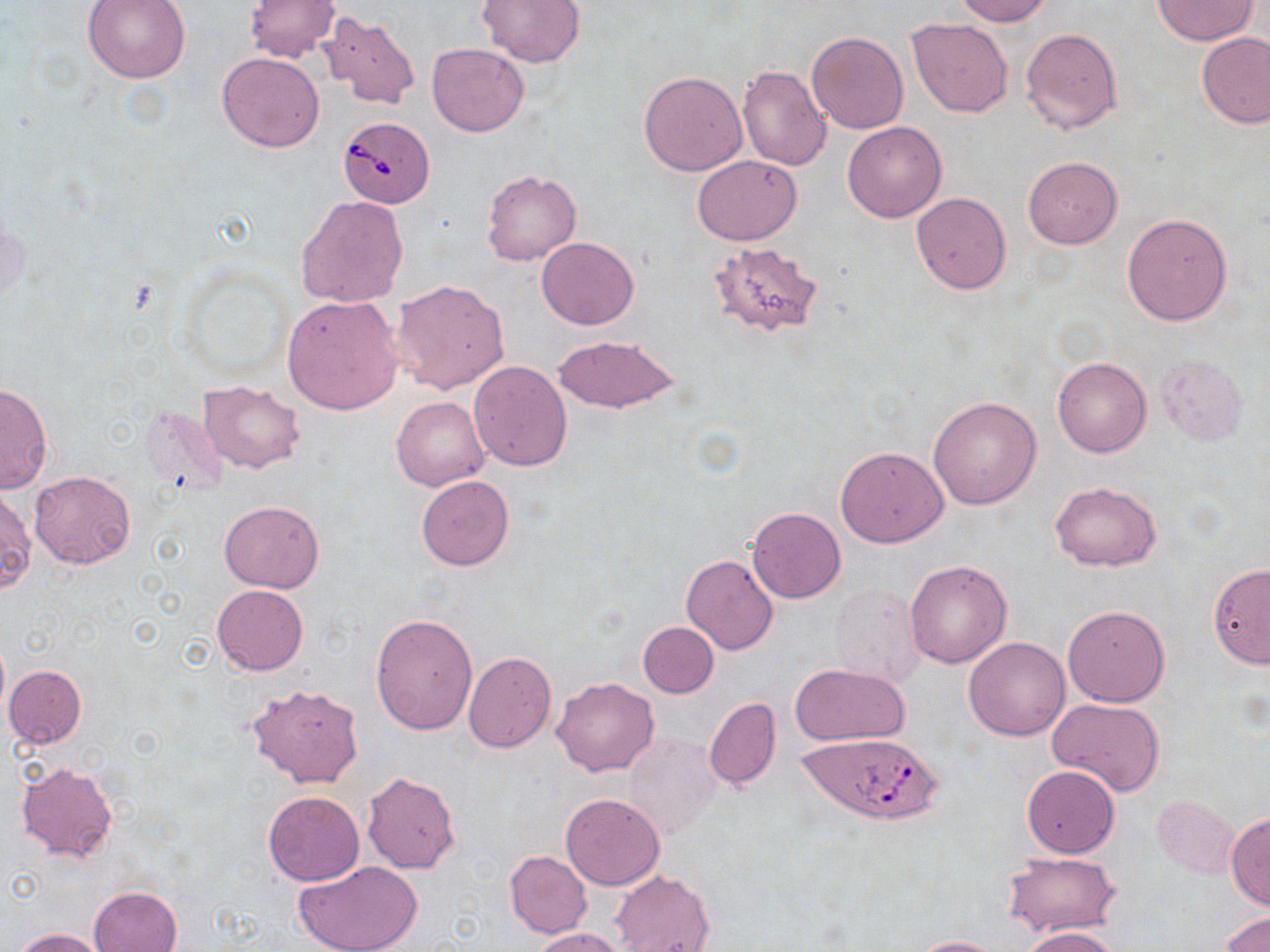

Summary:
  - Coordinate format: approximate bounding boxes as named x1/y1/x2/y2 corners in pixels
  - Babesia divergens-infected red blood cell locations: (x1=339, y1=116, x2=436, y2=208), (x1=800, y1=734, x2=941, y2=825)
  - Uninfected red blood cell locations: (x1=83, y1=0, x2=190, y2=83), (x1=244, y1=0, x2=339, y2=63), (x1=479, y1=0, x2=584, y2=68), (x1=954, y1=0, x2=1051, y2=25), (x1=1151, y1=1, x2=1257, y2=45), (x1=315, y1=12, x2=421, y2=108), (x1=907, y1=18, x2=1013, y2=118), (x1=1021, y1=28, x2=1122, y2=134), (x1=807, y1=31, x2=908, y2=134), (x1=1197, y1=32, x2=1270, y2=129), (x1=427, y1=43, x2=529, y2=136), (x1=217, y1=52, x2=326, y2=152), (x1=738, y1=64, x2=832, y2=171), (x1=639, y1=70, x2=747, y2=176), (x1=842, y1=121, x2=947, y2=222), (x1=693, y1=155, x2=802, y2=245), (x1=1023, y1=156, x2=1122, y2=248), (x1=482, y1=170, x2=582, y2=266), (x1=910, y1=192, x2=1011, y2=293), (x1=296, y1=195, x2=408, y2=307), (x1=1122, y1=214, x2=1232, y2=326), (x1=536, y1=237, x2=639, y2=330), (x1=709, y1=241, x2=825, y2=337), (x1=391, y1=279, x2=510, y2=395), (x1=281, y1=296, x2=403, y2=414), (x1=551, y1=336, x2=681, y2=414), (x1=1155, y1=354, x2=1249, y2=446), (x1=1052, y1=357, x2=1152, y2=458), (x1=467, y1=360, x2=573, y2=472), (x1=0, y1=380, x2=53, y2=493), (x1=198, y1=380, x2=306, y2=473), (x1=391, y1=396, x2=489, y2=490), (x1=928, y1=396, x2=1040, y2=510), (x1=836, y1=445, x2=948, y2=548), (x1=30, y1=470, x2=136, y2=569), (x1=416, y1=475, x2=513, y2=571), (x1=1050, y1=481, x2=1161, y2=571), (x1=0, y1=487, x2=34, y2=594), (x1=219, y1=500, x2=324, y2=593), (x1=747, y1=507, x2=845, y2=603), (x1=681, y1=555, x2=778, y2=654), (x1=905, y1=558, x2=1012, y2=668), (x1=1208, y1=562, x2=1270, y2=668), (x1=212, y1=584, x2=308, y2=675), (x1=829, y1=584, x2=926, y2=687), (x1=1062, y1=604, x2=1169, y2=708), (x1=372, y1=613, x2=477, y2=736), (x1=638, y1=623, x2=719, y2=698), (x1=964, y1=637, x2=1069, y2=740), (x1=463, y1=651, x2=557, y2=752), (x1=790, y1=663, x2=910, y2=746), (x1=4, y1=666, x2=86, y2=749), (x1=552, y1=677, x2=659, y2=776), (x1=246, y1=683, x2=365, y2=788), (x1=703, y1=698, x2=781, y2=790), (x1=1046, y1=698, x2=1165, y2=798), (x1=624, y1=734, x2=721, y2=839), (x1=16, y1=762, x2=118, y2=862), (x1=1022, y1=764, x2=1120, y2=857), (x1=360, y1=772, x2=460, y2=873), (x1=262, y1=790, x2=364, y2=885), (x1=560, y1=793, x2=665, y2=890), (x1=1152, y1=797, x2=1238, y2=877), (x1=1226, y1=812, x2=1270, y2=910), (x1=505, y1=850, x2=591, y2=937), (x1=1005, y1=852, x2=1119, y2=938), (x1=293, y1=860, x2=426, y2=952), (x1=611, y1=870, x2=714, y2=952), (x1=89, y1=886, x2=182, y2=952), (x1=1219, y1=912, x2=1270, y2=952), (x1=1021, y1=926, x2=1122, y2=952), (x1=530, y1=927, x2=626, y2=952), (x1=10, y1=928, x2=108, y2=951), (x1=909, y1=936, x2=1007, y2=952)
  - Slide-level diagnosis: Babesia divergens
  - Image size: 1270×952 pixels
  - Preparation: thin blood film
  - Field of view: one of a larger specimen
  - Magnification: 1000x
  - Stain: May-Grünwald-Giemsa
  - Modality: optical microscopy